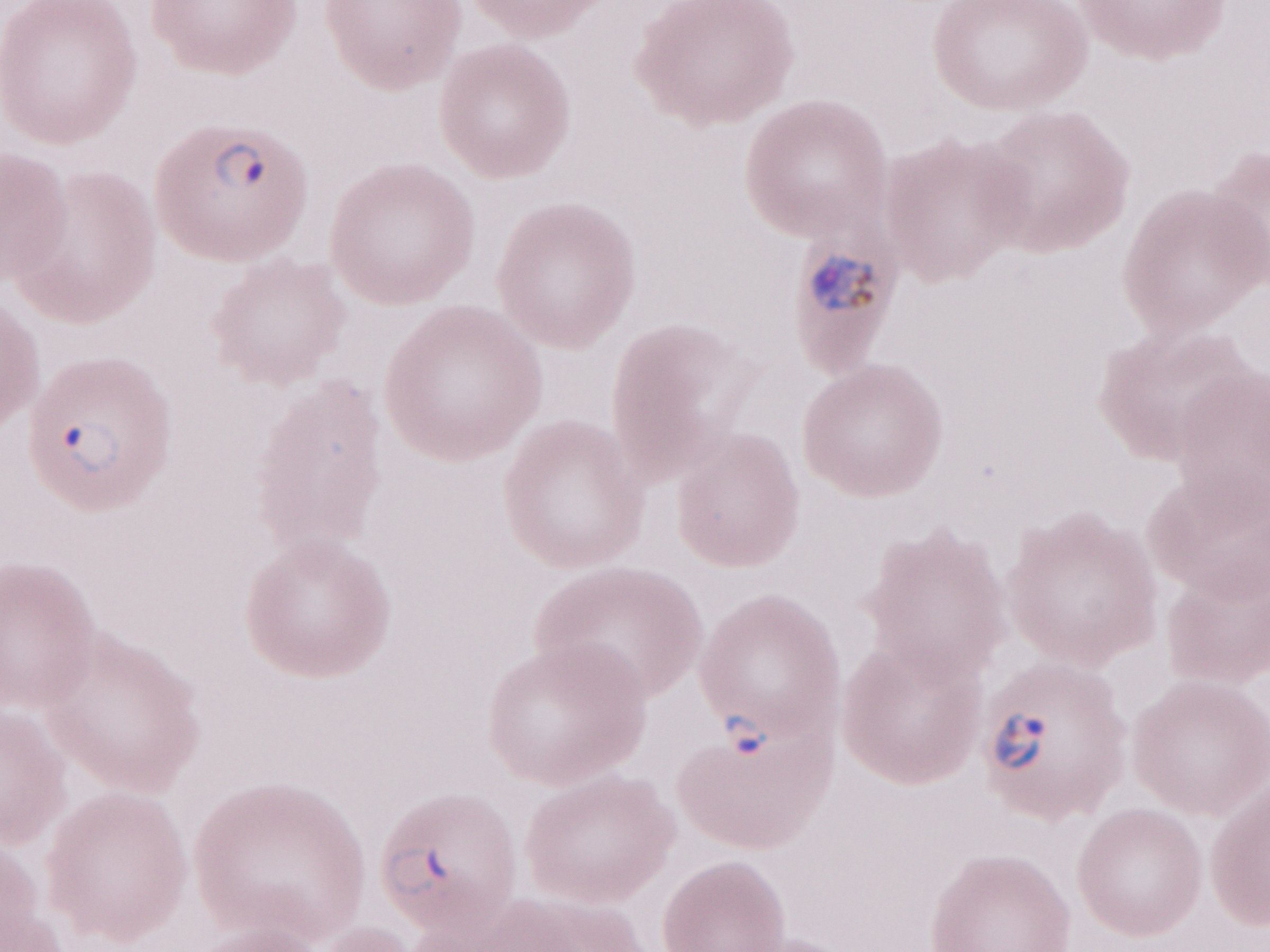 One field of this slide. Image is 1270×952 pixels. May-Grünwald-Giemsa (MGG) stain. Thin peripheral-blood smear. 1,000x magnification. Patient-level malaria diagnosis: positive. Olympus BX43 microscope and DP73 digital camera.